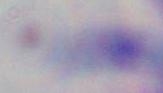

identification = Toxoplasma gondii
modality = photomicrograph
magnification = 1000x